Assess this cell for malaria.
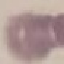

It is uninfected.

stain: Giemsa
preparation: thin blood smear
image_type: automatically extracted cell patch, resized to 64 × 64 pixels
capture: smartphone through the microscope eyepiece